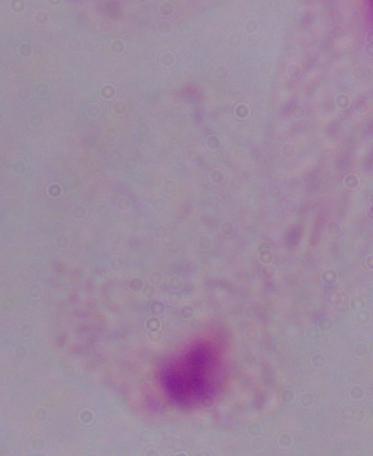
identification = trichomonad
modality = photomicrograph
magnification = 1000x